Give the position of every malaria parasite.
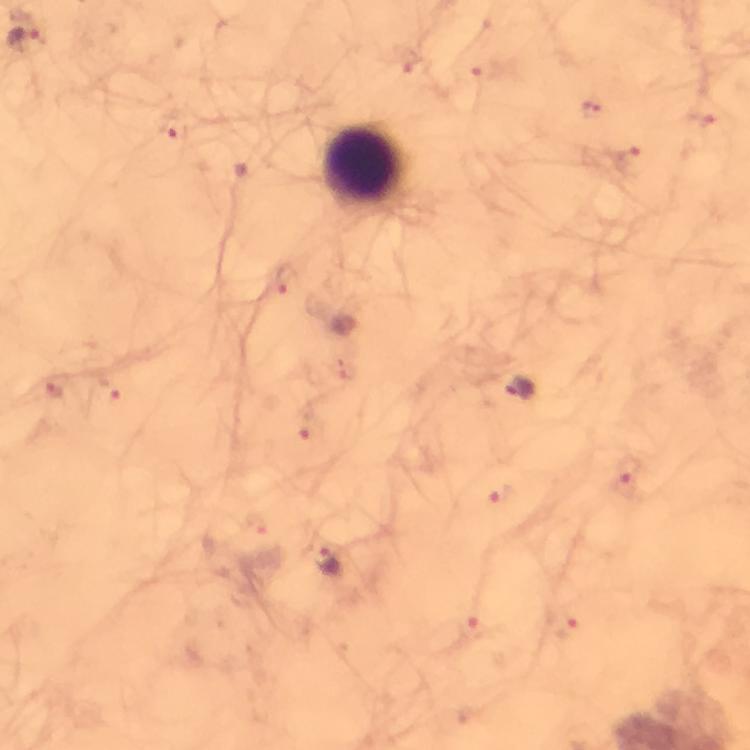

Approximate object centers, in pixels from the top-left corner.
Malaria parasites: (x=27, y=41), (x=590, y=110), (x=703, y=122), (x=175, y=130), (x=631, y=162), (x=283, y=277), (x=520, y=387), (x=54, y=388), (x=109, y=392), (x=306, y=427), (x=626, y=471), (x=500, y=494), (x=326, y=560), (x=569, y=627), (x=474, y=630).

Leukocyte locations: (x=364, y=168). Immersion oil applied. From a diagnostic examination for malaria. Giemsa-stained preparation. Smartphone photograph taken through a microscope. Cropped region of a single field of view. Image is 750×750 pixels. 100x magnification. Thick smear.